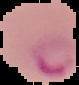
Summary:
  - Image size: 79×85 pixels
  - Preparation: thin blood film
  - Image type: segmented cell region on a black background
  - Result: Plasmodium parasites detected